Report the malaria status of this cell.
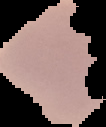
It is uninfected.

image type = cell region segmented out of the field of view; surrounding area masked to black
image size = 106×127 pixels
preparation = thin blood film